Name the cell type shown.
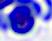
This is a leukocyte.

Micrograph. 400x magnification.